Name the blood parasite species.
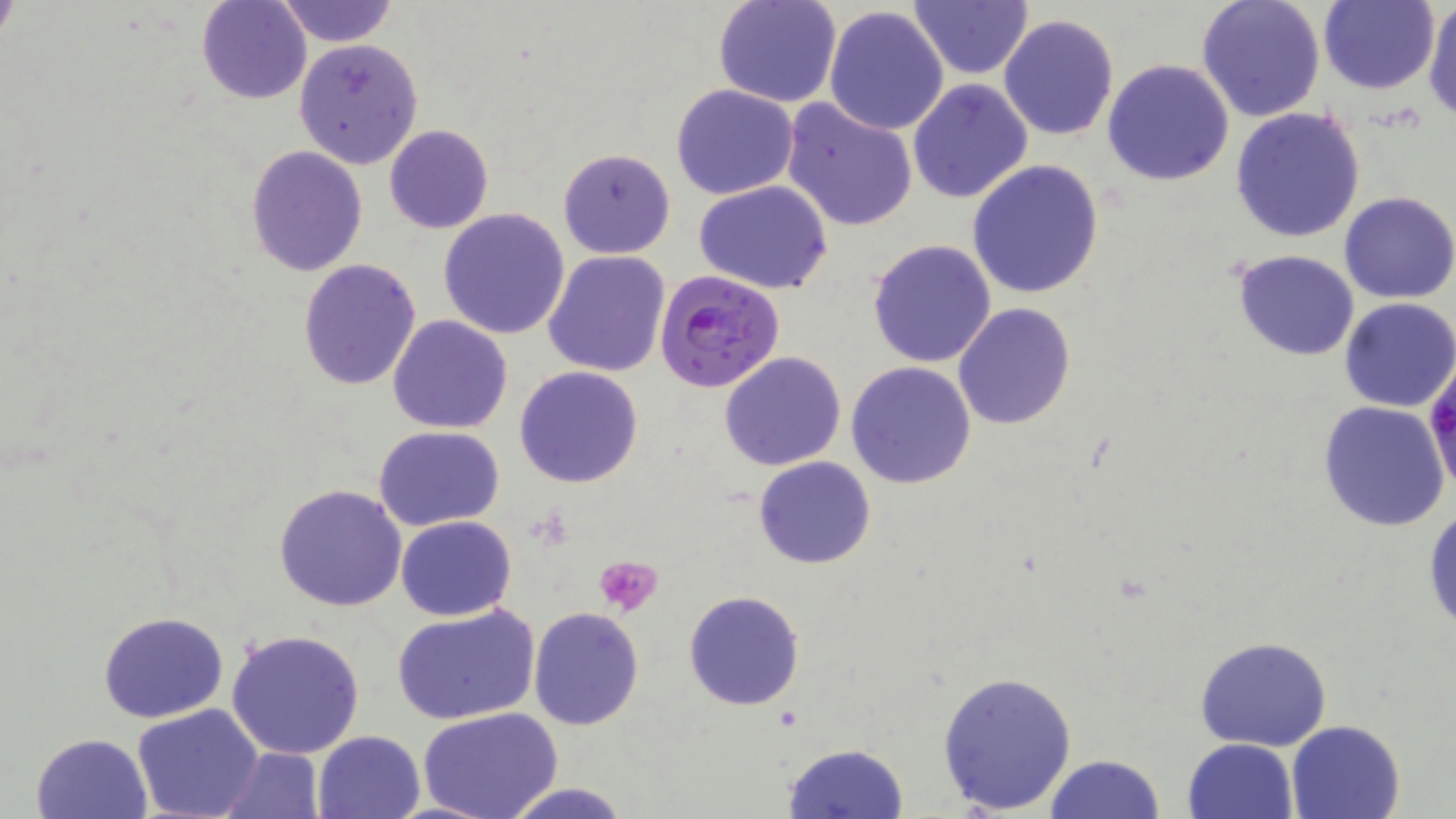
Plasmodium falciparum.

Approximate bounding boxes as (x1,y1)-(x2,y2) corner pairs in pixels. Platelet locations: (595,555)-(663,618). Uninfected red blood cell locations: (196,0)-(311,104), (274,0)-(400,48), (712,0)-(842,108), (908,0)-(1034,81), (1195,0)-(1326,122), (1424,0)-(1456,121), (1317,1)-(1440,95), (822,5)-(949,137), (999,12)-(1120,141), (292,38)-(424,170), (1102,58)-(1236,187), (908,80)-(1033,204), (671,84)-(799,200), (780,97)-(919,233), (1230,107)-(1366,245), (385,124)-(493,234), (244,146)-(369,278), (557,147)-(676,258), (967,161)-(1104,299), (694,182)-(835,295), (1338,192)-(1456,304), (438,209)-(571,339), (866,239)-(998,368), (1229,249)-(1361,361), (542,250)-(669,377), (296,258)-(421,392), (1338,298)-(1456,413), (952,301)-(1075,430), (387,315)-(513,435), (719,350)-(847,470), (846,361)-(977,488), (514,366)-(644,487), (1317,401)-(1450,532), (374,425)-(505,531), (754,455)-(875,569), (273,483)-(408,612), (1424,504)-(1456,633), (395,516)-(517,620), (683,590)-(804,711), (390,604)-(541,726), (529,606)-(644,730), (98,611)-(229,723), (225,628)-(368,759), (1194,635)-(1332,751), (936,670)-(1077,814), (131,704)-(263,818), (419,709)-(563,819), (1285,719)-(1406,819), (314,730)-(425,819), (31,731)-(152,817), (1183,738)-(1298,819), (782,742)-(909,819), (219,747)-(323,818), (1044,754)-(1166,819), (500,780)-(633,819). Plasmodium falciparum-infected red blood cell locations: (654,268)-(786,394). Image is 1456×819 pixels. Thin blood film. 1000x magnification. May-Grünwald-Giemsa stain. Light microscopy. Single field of view.